Give the extent of all Plasmodium malariae-infected red blood cells.
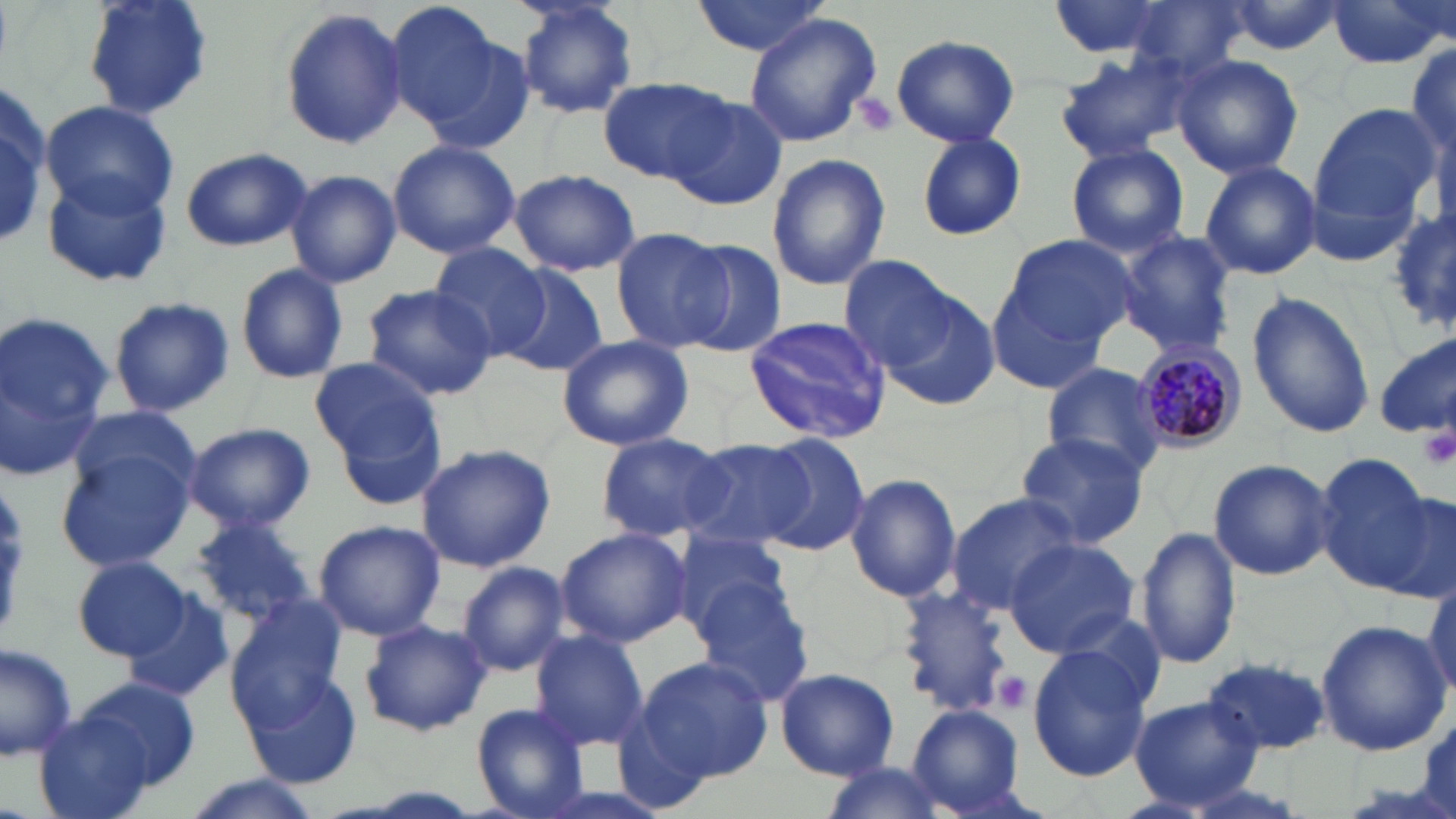

Approximate bounding boxes as (x1,y1)-(x2,y2) corner pairs in pixels.
Plasmodium malariae-infected red blood cells: (1135,342)-(1245,451).

Summary:
  - Uninfected red blood cell locations: (81,0)-(213,122), (512,0)-(640,120), (690,0)-(831,58), (1043,0)-(1183,61), (1222,0)-(1347,57), (1122,1)-(1252,85), (1327,1)-(1454,69), (387,2)-(513,138), (278,8)-(409,149), (745,15)-(883,144), (890,34)-(1020,147), (1407,42)-(1456,165), (1049,48)-(1197,162), (1172,55)-(1303,177), (597,75)-(738,185), (0,78)-(51,251), (664,93)-(791,209), (38,100)-(180,220), (0,102)-(53,242), (1310,105)-(1446,228), (916,132)-(1027,241), (386,139)-(520,259), (1064,142)-(1189,258), (180,146)-(313,252), (766,153)-(891,290), (1199,159)-(1321,280), (42,168)-(175,290), (509,168)-(640,277), (284,170)-(401,287), (1389,211)-(1455,337), (611,227)-(734,353), (1117,231)-(1237,354), (1001,233)-(1139,348), (678,241)-(789,358), (428,244)-(554,359), (841,256)-(959,370), (235,262)-(349,385), (501,265)-(609,377), (361,283)-(498,401), (991,285)-(1109,394), (1246,290)-(1376,439), (885,291)-(999,411), (109,295)-(234,419), (0,310)-(113,481), (743,315)-(892,445), (555,335)-(694,451), (1375,336)-(1455,438), (309,355)-(439,464), (1040,362)-(1169,481), (328,389)-(450,513), (67,408)-(203,506), (182,422)-(317,532), (1015,432)-(1148,549), (595,433)-(734,542), (754,433)-(870,555), (682,438)-(811,552), (415,443)-(555,572), (56,449)-(195,572), (1316,455)-(1439,594), (1208,458)-(1335,579), (845,472)-(960,603), (1369,488)-(1455,601), (946,492)-(1082,613), (186,515)-(319,628), (313,519)-(443,641), (1135,525)-(1241,669), (555,527)-(692,647), (669,527)-(794,638), (1002,538)-(1139,657), (74,555)-(193,660), (457,561)-(570,677), (1422,572)-(1455,702), (690,579)-(816,708), (895,587)-(1016,715), (120,593)-(234,705), (226,596)-(346,727), (359,620)-(491,738), (1316,620)-(1450,757), (528,629)-(650,753), (0,642)-(76,763), (1028,644)-(1150,779), (635,656)-(771,784), (1200,657)-(1333,755), (776,667)-(899,780), (243,671)-(361,789), (75,678)-(201,791), (1129,697)-(1263,811), (471,705)-(592,818), (907,705)-(1027,814), (32,709)-(161,819), (819,762)-(953,816), (177,777)-(321,819)
  - Platelet locations: (852,89)-(899,139), (1420,428)-(1456,470), (993,672)-(1033,713)
  - Slide-level diagnosis: Plasmodium malariae
  - Modality: light microscopy
  - Preparation: thin blood film
  - Image size: 1456×819 pixels
  - Stain: May-Grünwald-Giemsa
  - Field of view: single
  - Magnification: 1000x